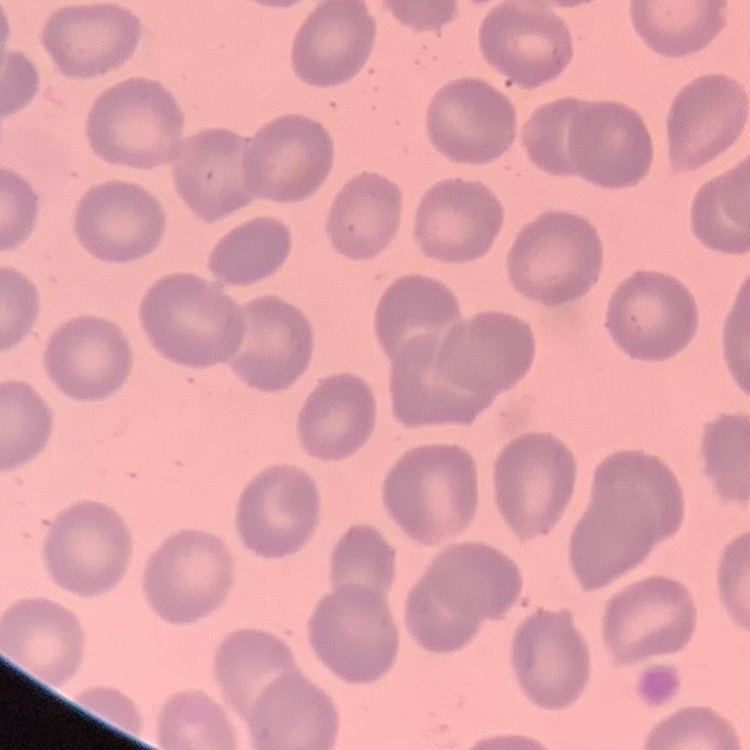

{
  "red_blood_cell_morphology": "no rouleaux formation",
  "preparation": "thin blood film",
  "image_type": "one tile cut from a larger photomicrograph",
  "stain": "Field's or Giemsa"
}